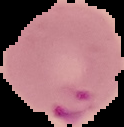
Summary:
  - Image size: 124×127 pixels
  - Image type: cell region segmented out of the field of view; surrounding area masked to black
  - Malaria status: parasitized
  - Preparation: thin blood film